Report the malaria status of this cell.
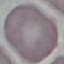

Uninfected.

capture = smartphone camera at the microscope eyepiece
preparation = thin smear
image type = automatically extracted cell patch, resized to 64 × 64 pixels
stain = Giemsa